Identify the parasite.
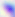

Toxoplasma gondii.

Micrograph. Captured at 400x magnification.